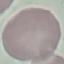 Malaria status: uninfected. Thin blood film. Cell patch, automatically extracted from a larger field of view and resized to 64 × 64 pixels. Acquired by smartphone through the microscope eyepiece. Giemsa-stained preparation.